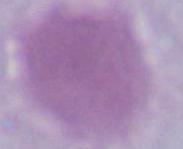
Summary:
  - Modality: micrograph
  - Magnification: 1000x
  - Identification: erythrocyte